Report the malaria status of this cell.
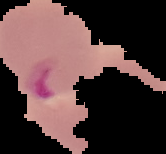
Parasitized.

Summary:
  - Image type: cell region segmented out of the field of view; surrounding area masked to black
  - Preparation: thin blood smear
  - Image size: 166×154 pixels